Locate and identify every blood parasite.
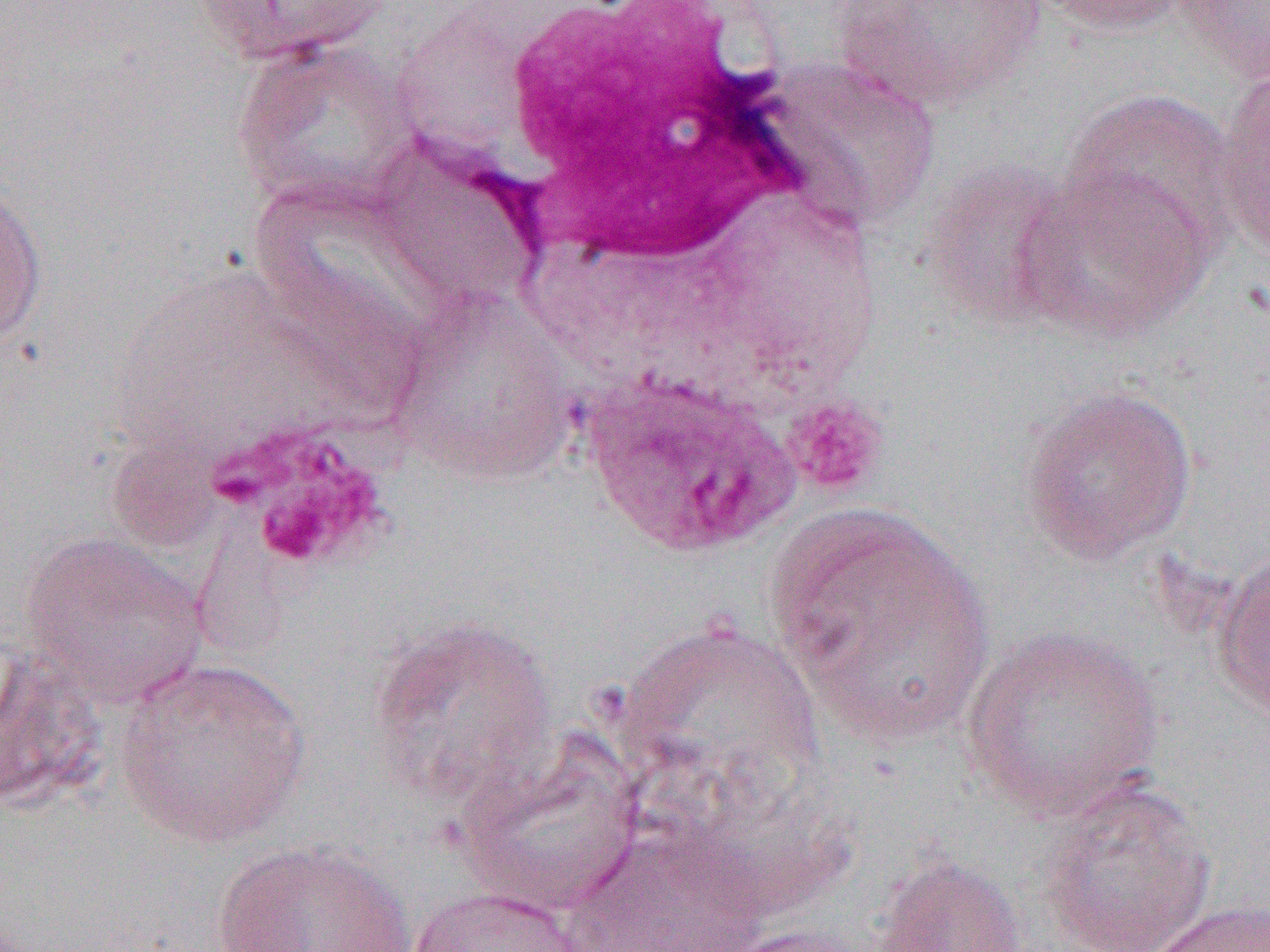
Approximate bounding boxes as named x1/y1/x2/y2 corners in pixels.
Plasmodium ovale-infected red blood cells: (x1=582, y1=372, x2=800, y2=559).
No Plasmodium falciparum, Plasmodium malariae, Plasmodium vivax, Babesia divergens, or Trypanosoma brucei observed.

slide_level_diagnosis: Plasmodium ovale
uninfected_red_blood_cell_locations: 'approximate bounding boxes as named x1/y1/x2/y2 corners in pixels: (x1=186, y1=0, x2=398, y2=67), (x1=1033, y1=0, x2=1197, y2=37), (x1=1176, y1=0, x2=1270, y2=83), (x1=832, y1=1, x2=1045, y2=111), (x1=229, y1=35, x2=425, y2=213), (x1=762, y1=58, x2=941, y2=228), (x1=1213, y1=62, x2=1270, y2=264), (x1=1061, y1=88, x2=1240, y2=255), (x1=920, y1=162, x2=1082, y2=328), (x1=1013, y1=167, x2=1215, y2=343), (x1=0, y1=174, x2=48, y2=356), (x1=388, y1=290, x2=579, y2=483), (x1=1020, y1=383, x2=1199, y2=565), (x1=764, y1=499, x2=997, y2=748), (x1=20, y1=532, x2=209, y2=709), (x1=1213, y1=548, x2=1270, y2=723), (x1=366, y1=615, x2=561, y2=809), (x1=612, y1=619, x2=826, y2=822), (x1=961, y1=626, x2=1167, y2=819), (x1=0, y1=651, x2=111, y2=815), (x1=116, y1=656, x2=311, y2=848), (x1=454, y1=738, x2=644, y2=918), (x1=1036, y1=780, x2=1216, y2=952), (x1=563, y1=825, x2=769, y2=952), (x1=210, y1=840, x2=414, y2=952), (x1=871, y1=853, x2=1029, y2=952), (x1=405, y1=886, x2=589, y2=952), (x1=1145, y1=900, x2=1270, y2=952), (x1=705, y1=924, x2=876, y2=952)'
field_of_view: one of a larger specimen
modality: optical microscopy
preparation: thin blood smear
magnification: 1000x
platelet_locations: 'approximate bounding boxes as named x1/y1/x2/y2 corners in pixels: (x1=781, y1=393, x2=890, y2=501), (x1=222, y1=426, x2=400, y2=574)'
image_size: 1270×952 pixels